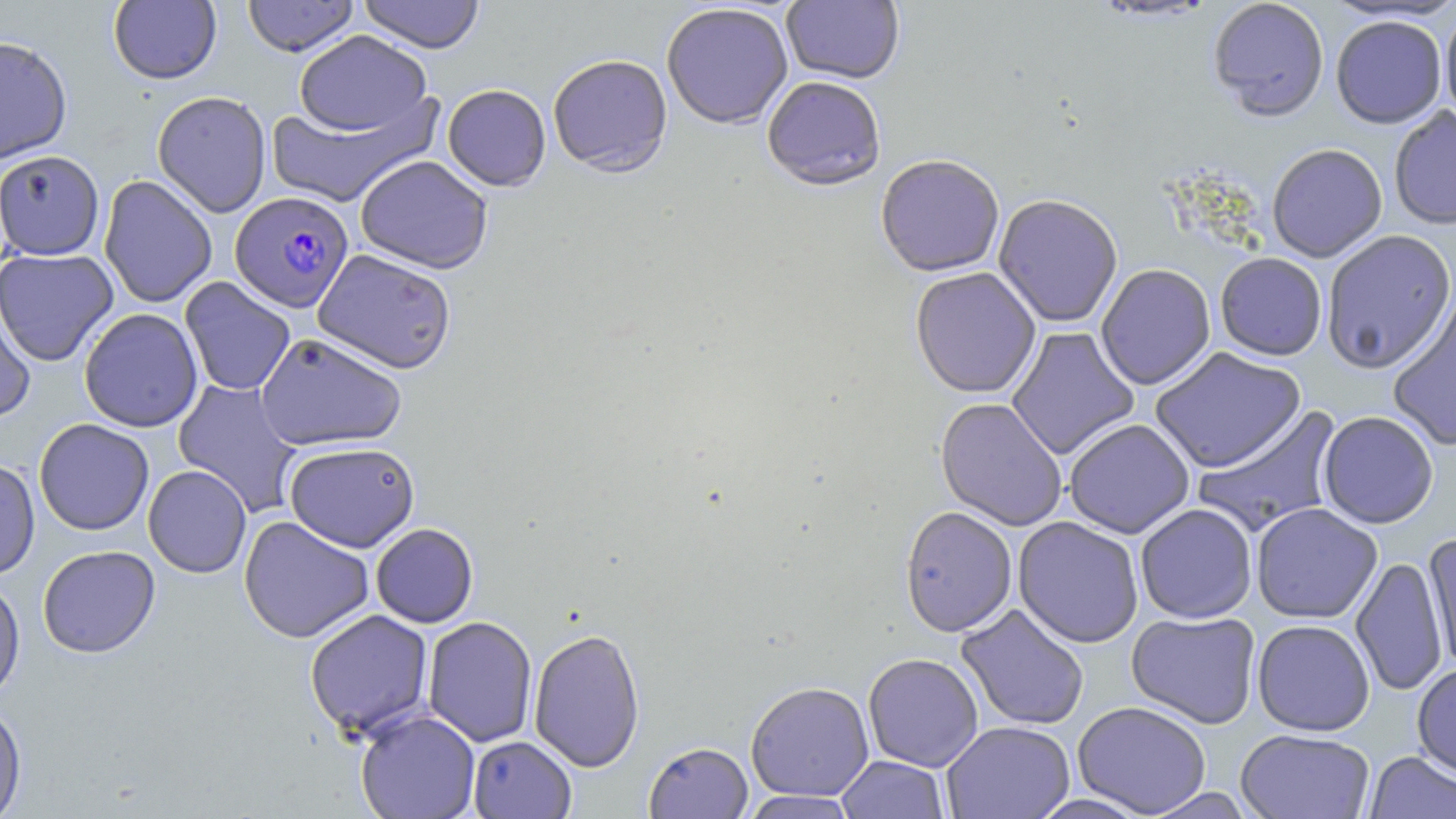

slide-level diagnosis = Plasmodium falciparum
image size = 1456×819 pixels
Plasmodium falciparum-infected red blood cell locations = approximate bounding boxes as (x1, y1, x2, y2) in pixels: (230, 191, 353, 312)
modality = optical microscopy
field of view = single
preparation = thin blood smear
magnification = 1000x
uninfected red blood cell locations = approximate bounding boxes as (x1, y1, x2, y2) in pixels: (242, 0, 359, 57), (357, 0, 485, 55), (781, 0, 905, 86), (1208, 0, 1329, 123), (108, 1, 221, 85), (661, 4, 793, 132), (1440, 6, 1456, 124), (1330, 16, 1448, 129), (293, 30, 434, 138), (0, 36, 72, 163), (548, 56, 673, 180), (761, 77, 886, 193), (442, 85, 551, 193), (152, 90, 272, 217), (265, 96, 439, 208), (1389, 106, 1456, 230), (1267, 144, 1387, 262), (0, 150, 105, 260), (355, 155, 493, 274), (875, 157, 1005, 278), (98, 175, 217, 308), (993, 195, 1123, 328), (1321, 230, 1456, 374), (0, 248, 118, 367), (312, 249, 457, 375), (1215, 253, 1327, 360), (1096, 264, 1216, 390), (910, 268, 1041, 399), (179, 276, 296, 396), (0, 287, 37, 423), (1387, 297, 1456, 452), (79, 308, 203, 432), (1006, 327, 1139, 461), (255, 332, 406, 452), (1150, 347, 1306, 473), (173, 378, 304, 517), (935, 398, 1068, 532), (1192, 406, 1344, 537), (1318, 411, 1439, 529), (34, 418, 154, 535), (1064, 419, 1194, 539), (283, 442, 420, 552), (0, 458, 40, 581), (143, 465, 252, 578), (1135, 503, 1257, 623), (1251, 503, 1382, 624), (899, 507, 1018, 637), (238, 515, 374, 643), (1013, 517, 1144, 648), (371, 523, 478, 628), (1421, 531, 1456, 676), (37, 545, 160, 658), (1350, 555, 1448, 697), (0, 575, 25, 703), (956, 604, 1090, 731), (304, 609, 434, 739), (1126, 611, 1262, 729), (422, 616, 538, 747), (1252, 619, 1375, 736), (529, 627, 645, 773), (863, 653, 983, 772), (1412, 662, 1456, 779), (745, 681, 874, 801), (0, 700, 27, 818), (1073, 701, 1212, 817), (355, 708, 480, 819), (941, 721, 1075, 819), (1235, 728, 1375, 819), (467, 735, 577, 818), (643, 741, 754, 818), (1365, 751, 1456, 818), (836, 755, 949, 819), (1142, 788, 1257, 818), (740, 790, 860, 818), (1026, 794, 1156, 819)
stain = May-Grünwald-Giemsa